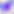

Micrograph. Toxoplasma gondii is seen. Captured at 400x magnification.